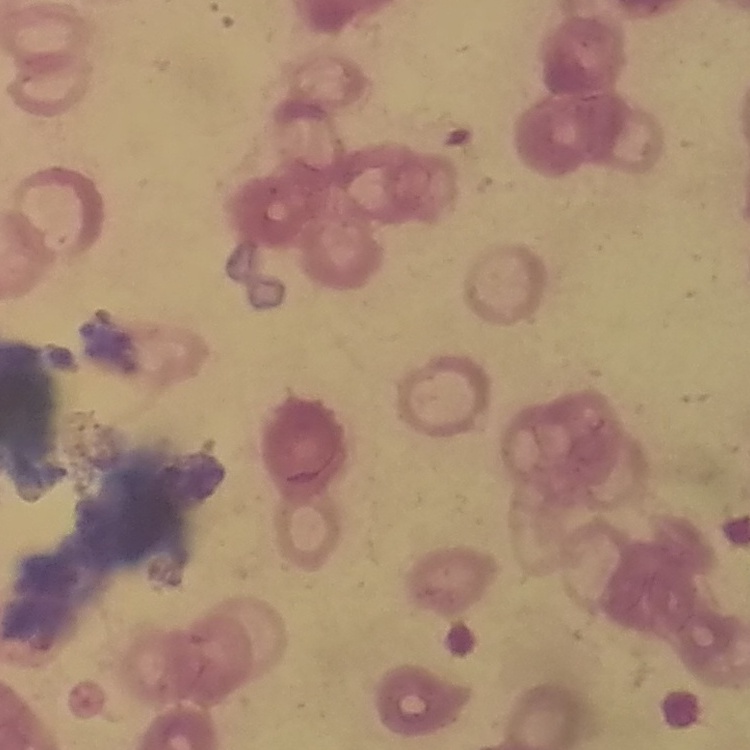

Summary:
  - Erythrocyte morphology: rouleaux formation
  - Image type: one tile cut from a larger photomicrograph
  - Preparation: thin blood smear
  - Stain: Field's or Giemsa